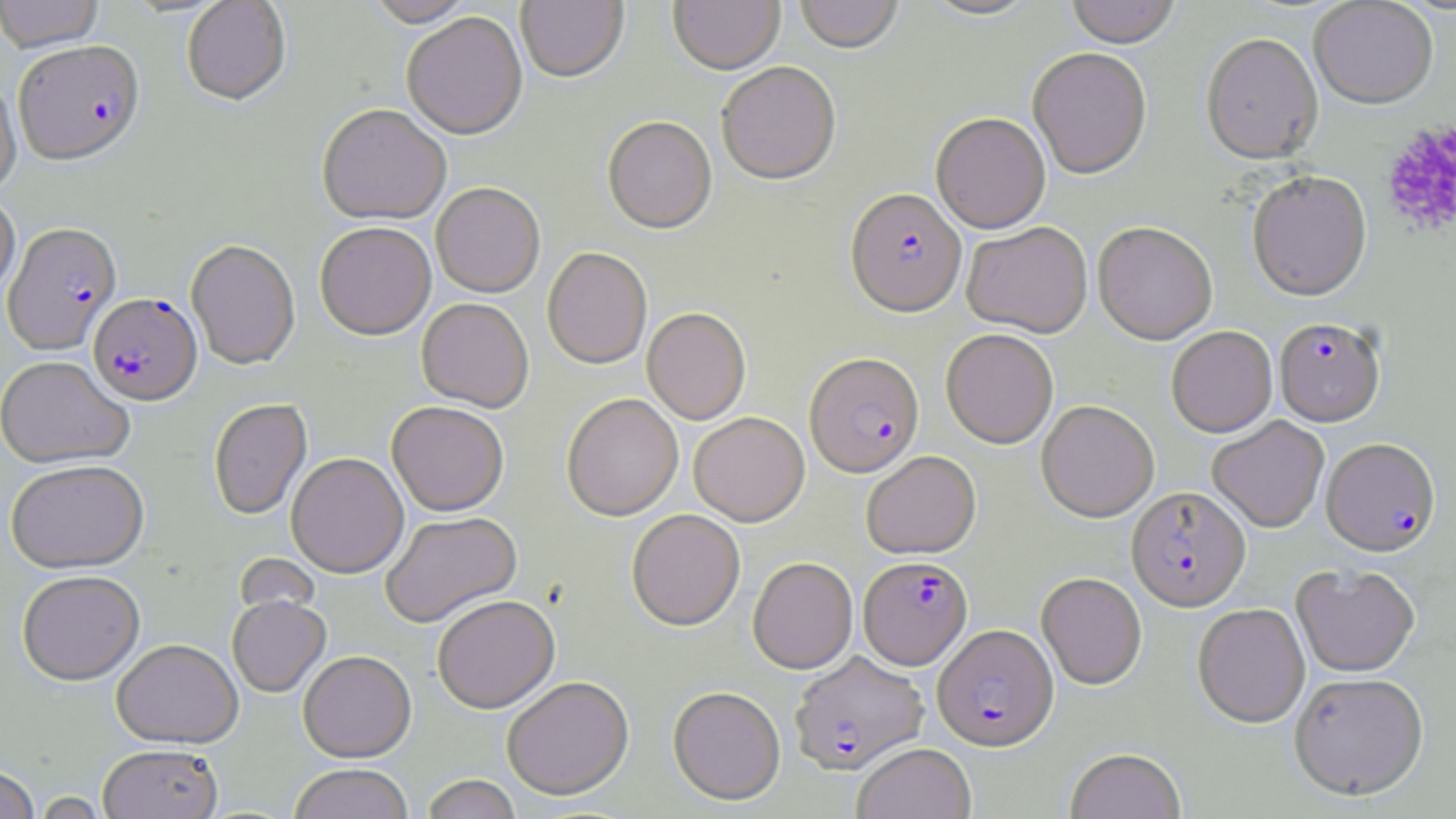
Approximate bounding boxes as [x1, y1, x2, y2] in pixels. Platelet locations: [1380, 122, 1456, 237]. Plasmodium falciparum-infected red blood cell locations: [14, 42, 146, 168], [845, 190, 967, 319], [3, 222, 122, 354], [88, 293, 203, 406], [1273, 319, 1386, 426], [805, 353, 924, 478], [1321, 439, 1440, 557], [1126, 487, 1251, 612], [859, 556, 974, 670], [933, 624, 1059, 751], [789, 651, 929, 776]. Uninfected red blood cell locations: [0, 0, 105, 52], [182, 0, 292, 108], [364, 0, 477, 29], [516, 0, 629, 85], [668, 0, 785, 76], [795, 0, 905, 56], [921, 0, 1042, 22], [1065, 0, 1180, 49], [1309, 1, 1438, 110], [402, 14, 528, 142], [1201, 35, 1323, 167], [1027, 48, 1152, 181], [717, 64, 841, 187], [0, 78, 22, 195], [317, 106, 451, 228], [931, 113, 1051, 234], [602, 118, 717, 236], [1247, 173, 1372, 303], [431, 185, 545, 299], [0, 191, 20, 303], [962, 223, 1093, 338], [1093, 223, 1218, 345], [315, 224, 436, 341], [186, 240, 300, 370], [542, 248, 652, 370], [416, 299, 534, 413], [642, 308, 751, 425], [1166, 326, 1277, 438], [941, 329, 1058, 449], [0, 356, 134, 470], [562, 394, 683, 522], [208, 399, 312, 521], [1037, 401, 1159, 522], [387, 402, 508, 517], [689, 413, 809, 526], [1207, 417, 1329, 532], [861, 451, 981, 560], [286, 453, 408, 578], [5, 460, 149, 573], [381, 511, 522, 629], [627, 511, 745, 631], [748, 557, 858, 675], [1291, 565, 1420, 678], [17, 571, 145, 686], [1036, 573, 1147, 690], [228, 596, 331, 698], [432, 597, 560, 714], [1193, 603, 1310, 728], [111, 639, 244, 749], [298, 651, 416, 763], [1289, 673, 1429, 802], [502, 677, 635, 802], [668, 687, 785, 806], [852, 743, 977, 819], [98, 744, 223, 819], [1065, 747, 1186, 819], [0, 764, 40, 819], [289, 764, 414, 819], [421, 775, 522, 819], [31, 792, 111, 818]. Slide-level diagnosis: Plasmodium falciparum. Image is 1456×819 pixels. May-Grünwald-Giemsa stain. One field of a larger specimen. 1000x magnification. Thin blood smear. Light microscopy.